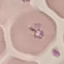 Malaria status: parasitized. Acquired by smartphone through the microscope eyepiece. Cell patch, automatically extracted from a larger field of view and resized to 64 × 64 pixels. Thin blood film. Giemsa stain.